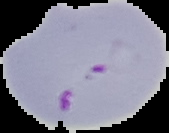

{
  "preparation": "thin blood film",
  "image_size": "169×133 pixels",
  "result": "malaria parasites identified",
  "image_type": "cell region segmented out of the field of view; surrounding area masked to black"
}